Assess this cell for malaria.
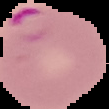

It is parasitized.

image size = 109×109 pixels
image type = segmented cell region with the area outside set to black
preparation = thin blood film